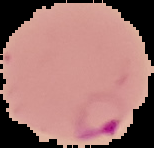
From a thin blood film. Image is 154×148 pixels. The area outside the segmented cell region is set to black. Result: malaria parasites detected.